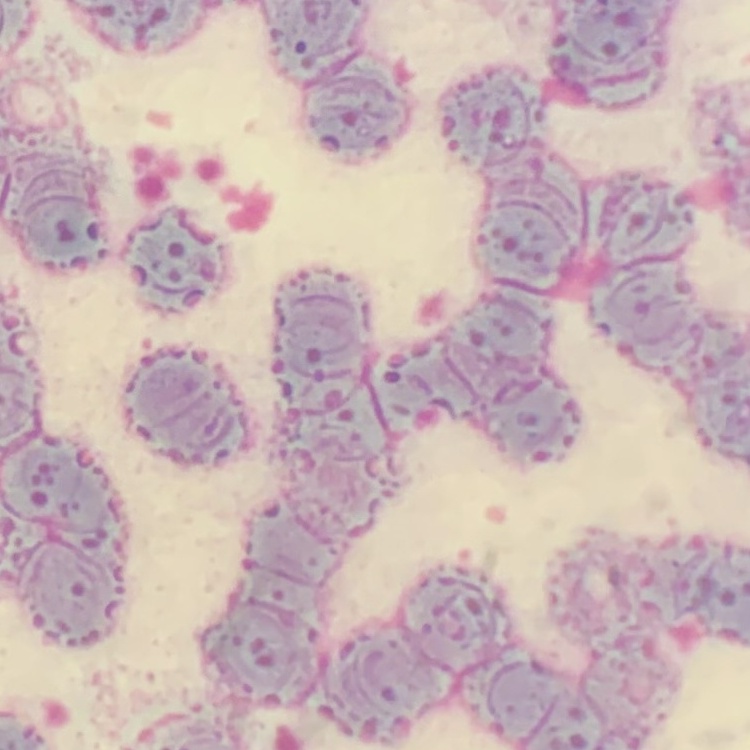
The red blood cells exhibit rouleaux formation. Square crop of a larger photomicrograph. Thin blood film. Field's or Giemsa stain.